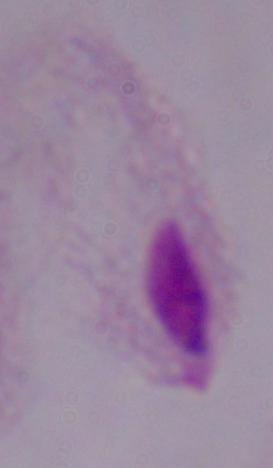
{
  "identification": "trichomonad",
  "modality": "micrograph",
  "magnification": "1000x"
}